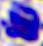
modality = photomicrograph
identification = white blood cell
magnification = 400x